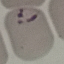

malaria status = parasitized
stain = Giemsa
image type = automatically extracted cell patch, resized to 64 × 64 pixels
capture = smartphone through the microscope eyepiece
preparation = thin smear